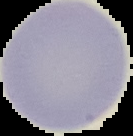

{
  "image_type": "cell region segmented out of the field of view; surrounding area masked to black",
  "result": "no malaria parasites detected",
  "image_size": "133×136 pixels",
  "preparation": "thin blood smear"
}